Assess this cell for malaria.
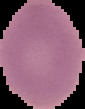
It is uninfected.

Summary:
  - Image type: cell region segmented out of the field of view; surrounding area masked to black
  - Image size: 85×109 pixels
  - Preparation: thin blood smear